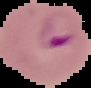
Summary:
  - Image size: 91×88 pixels
  - Malaria status: parasitized
  - Image type: segmented cell region with the area outside set to black
  - Preparation: thin blood smear